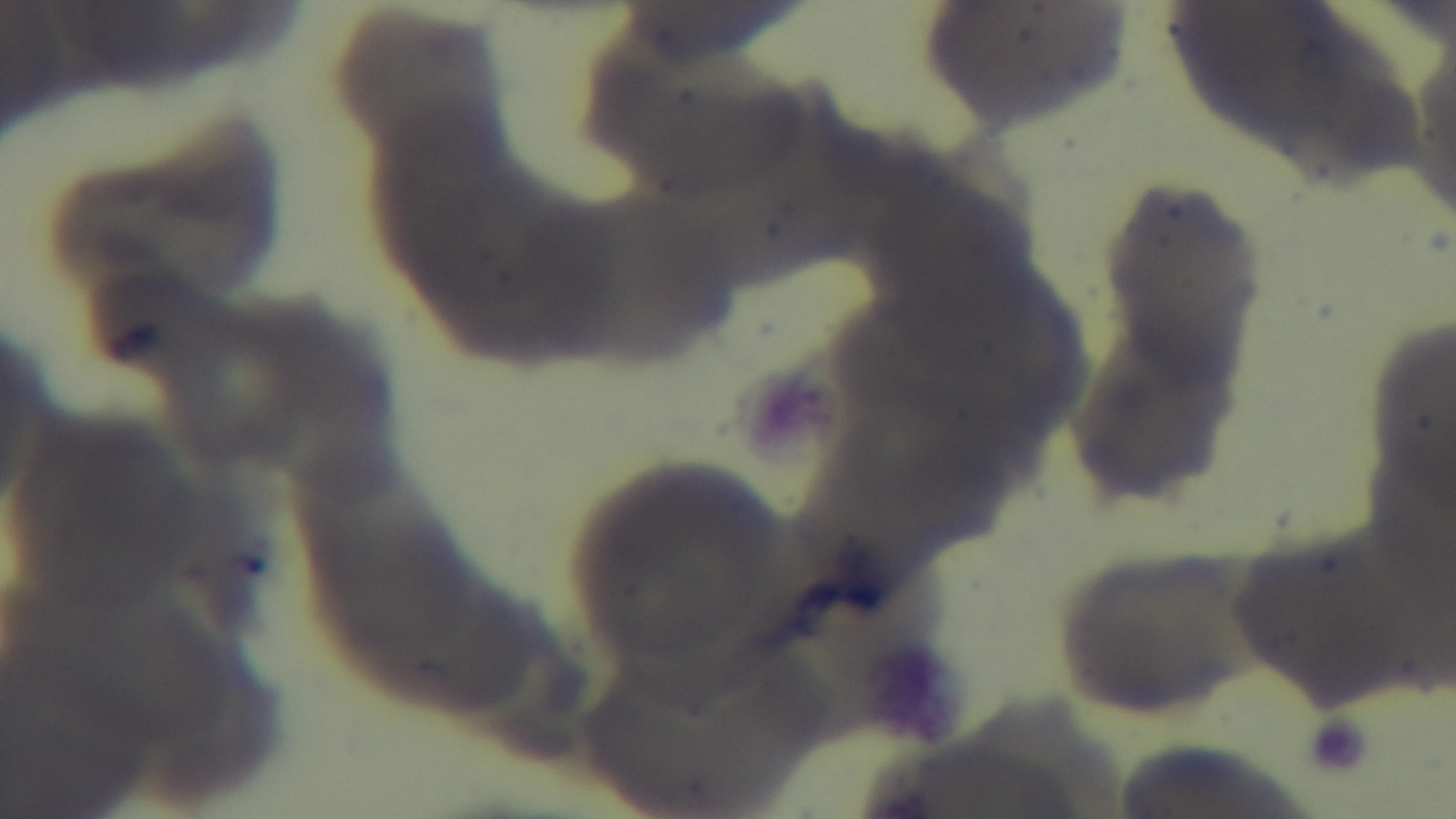
Summary:
  - Field of view: one from the slide
  - Capture: mounted 4K digital camera
  - Modality: light microscopy
  - Stain: Giemsa
  - Preparation: thin smear
  - Malaria status: negative
  - Objective: 100x oil immersion